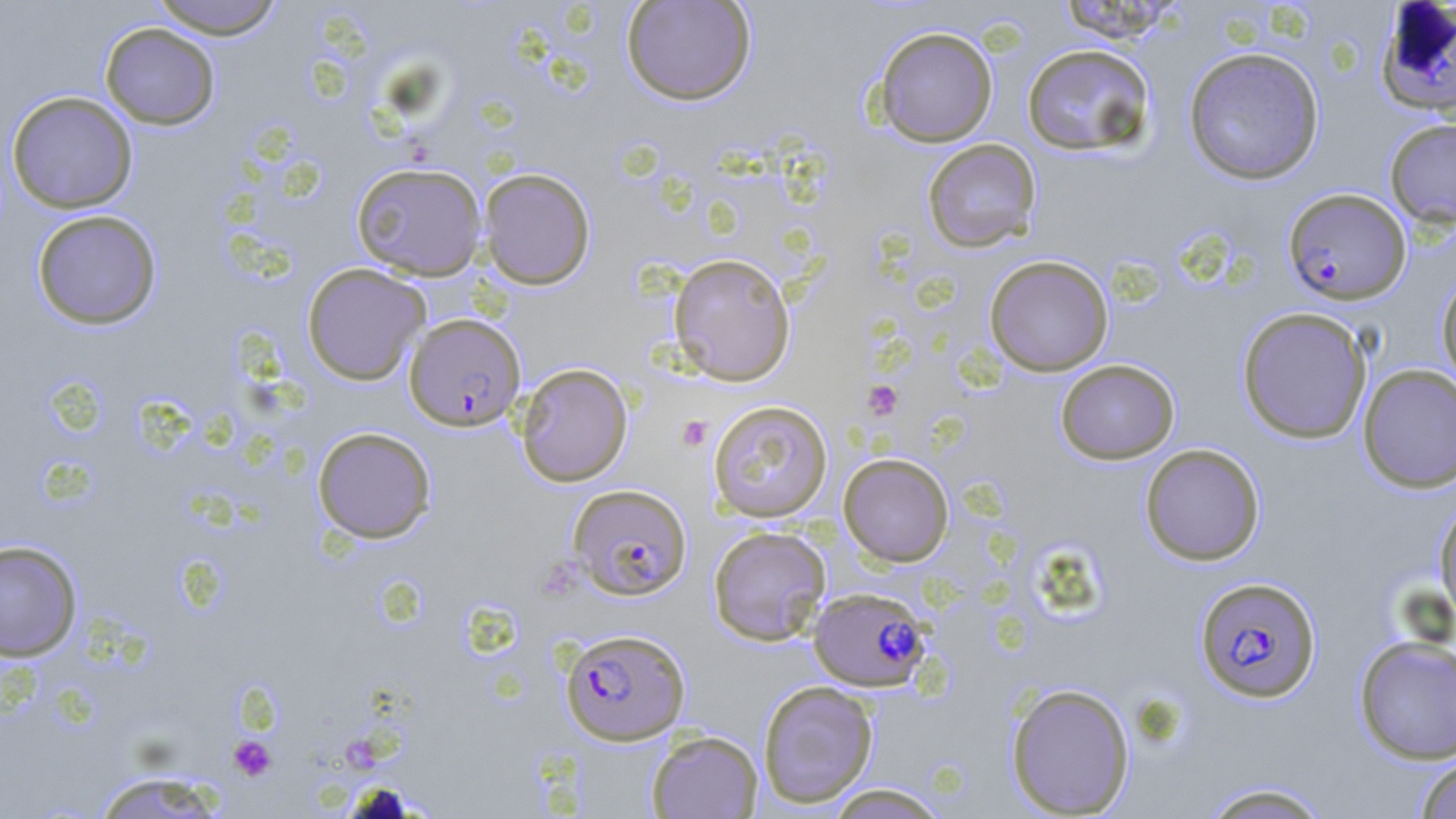
Approximate bounding boxes as (x1,y1)-(x2,y2) corner pairs in pixels. Uninfected red blood cell locations: (148,0)-(287,38), (621,0)-(756,105), (1053,1)-(1187,43), (99,22)-(220,129), (872,26)-(998,147), (1021,43)-(1156,156), (1183,46)-(1325,185), (6,90)-(138,213), (1384,118)-(1456,230), (922,138)-(1042,254), (350,161)-(487,280), (478,167)-(596,290), (31,209)-(162,329), (668,253)-(796,386), (984,255)-(1113,376), (301,262)-(430,385), (1436,270)-(1456,392), (1236,307)-(1373,444), (1055,359)-(1180,464), (516,363)-(633,487), (1358,364)-(1456,493), (708,400)-(833,522), (312,426)-(437,543), (1139,443)-(1265,566), (838,453)-(954,566), (1434,500)-(1456,626), (708,525)-(832,646), (0,540)-(83,662), (1353,634)-(1456,764), (757,680)-(879,808), (1005,682)-(1135,817), (646,730)-(763,818), (1413,754)-(1456,819), (90,770)-(229,818), (1196,782)-(1335,819), (822,783)-(952,818). Plasmodium falciparum-infected red blood cell locations: (1377,3)-(1456,117), (1283,188)-(1411,304), (404,313)-(526,431), (568,483)-(692,600), (1195,576)-(1321,703), (809,587)-(930,691), (560,628)-(690,745). Platelet locations: (862,380)-(903,420), (676,415)-(712,451), (228,735)-(277,781). Slide-level diagnosis: Plasmodium falciparum. 1000x magnification. May-Grünwald-Giemsa-stained preparation. Image is 1456×819 pixels. Single field of view. Optical microscopy. Thin blood film.